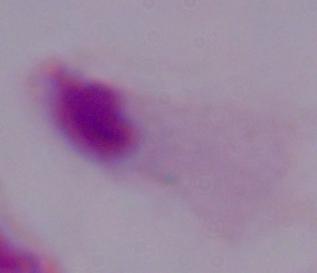

Summary:
  - Identification: trichomonad
  - Magnification: 1000x
  - Modality: micrograph